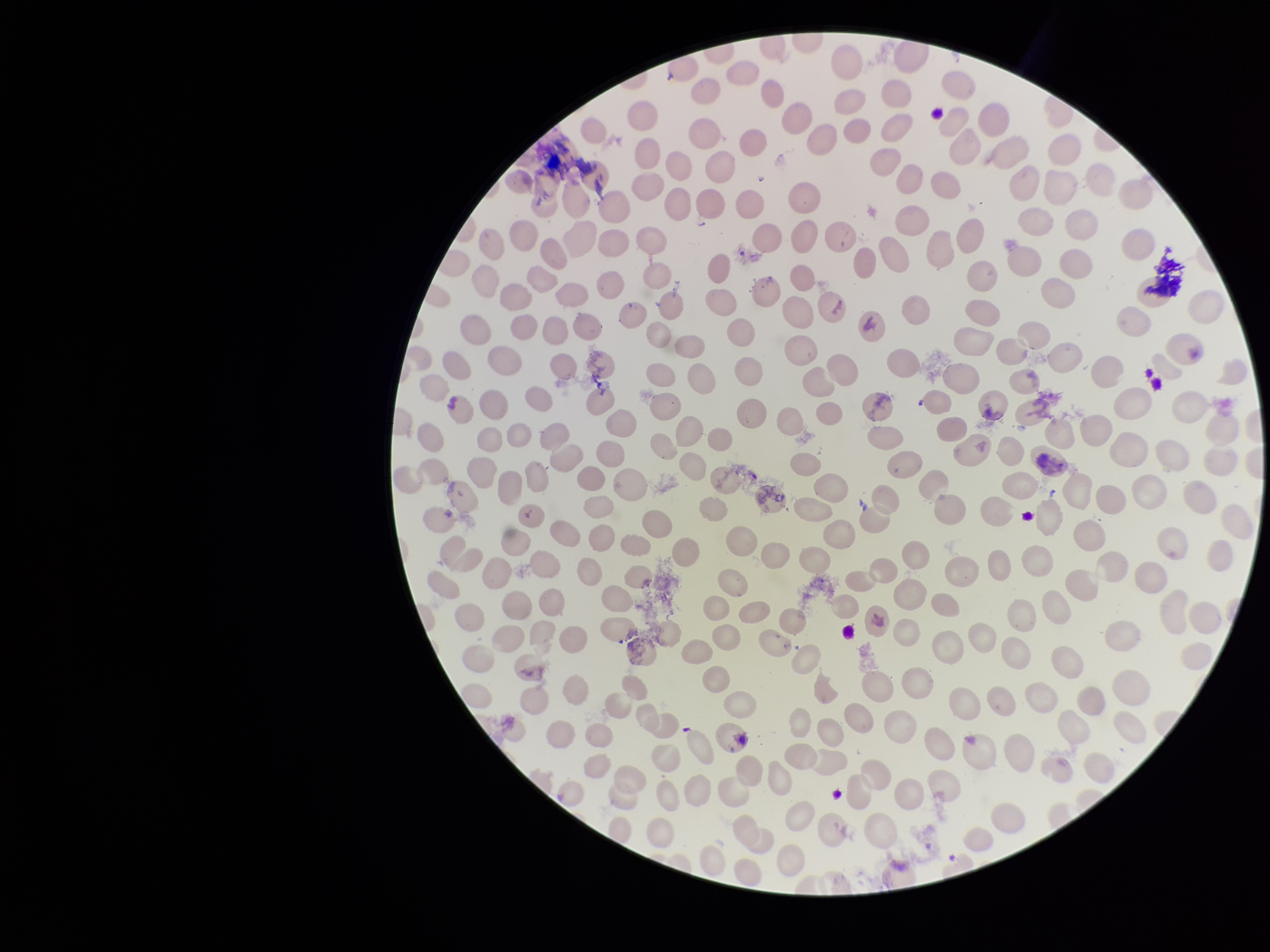

parasitized red blood cells = none identified
patient malaria status = positive
parasitized red blood cell count = 0
species reported for this patient = Plasmodium vivax
preparation = thin smear
stain = Giemsa
image size = 1270×952 pixels
capture = smartphone photograph through the microscope eyepiece
field of view = single
red blood cell count = 251